Describe the morphology of the red blood cells.
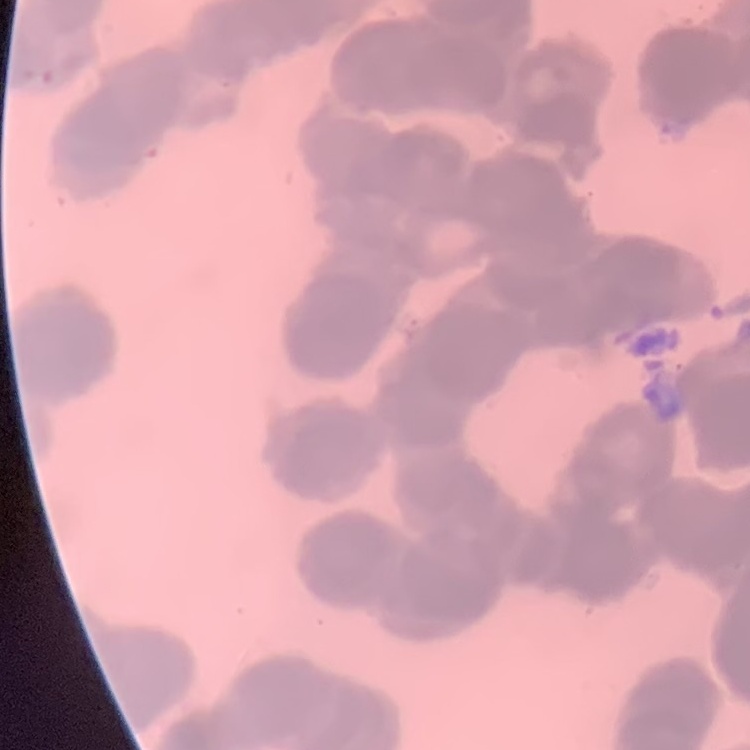

They show rouleaux formation.

Summary:
  - Stain: Field's or Giemsa
  - Preparation: thin blood smear
  - Image type: one tile cut from a larger photomicrograph